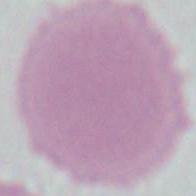
Summary:
  - Identification: red blood cell
  - Modality: micrograph
  - Magnification: 1000x